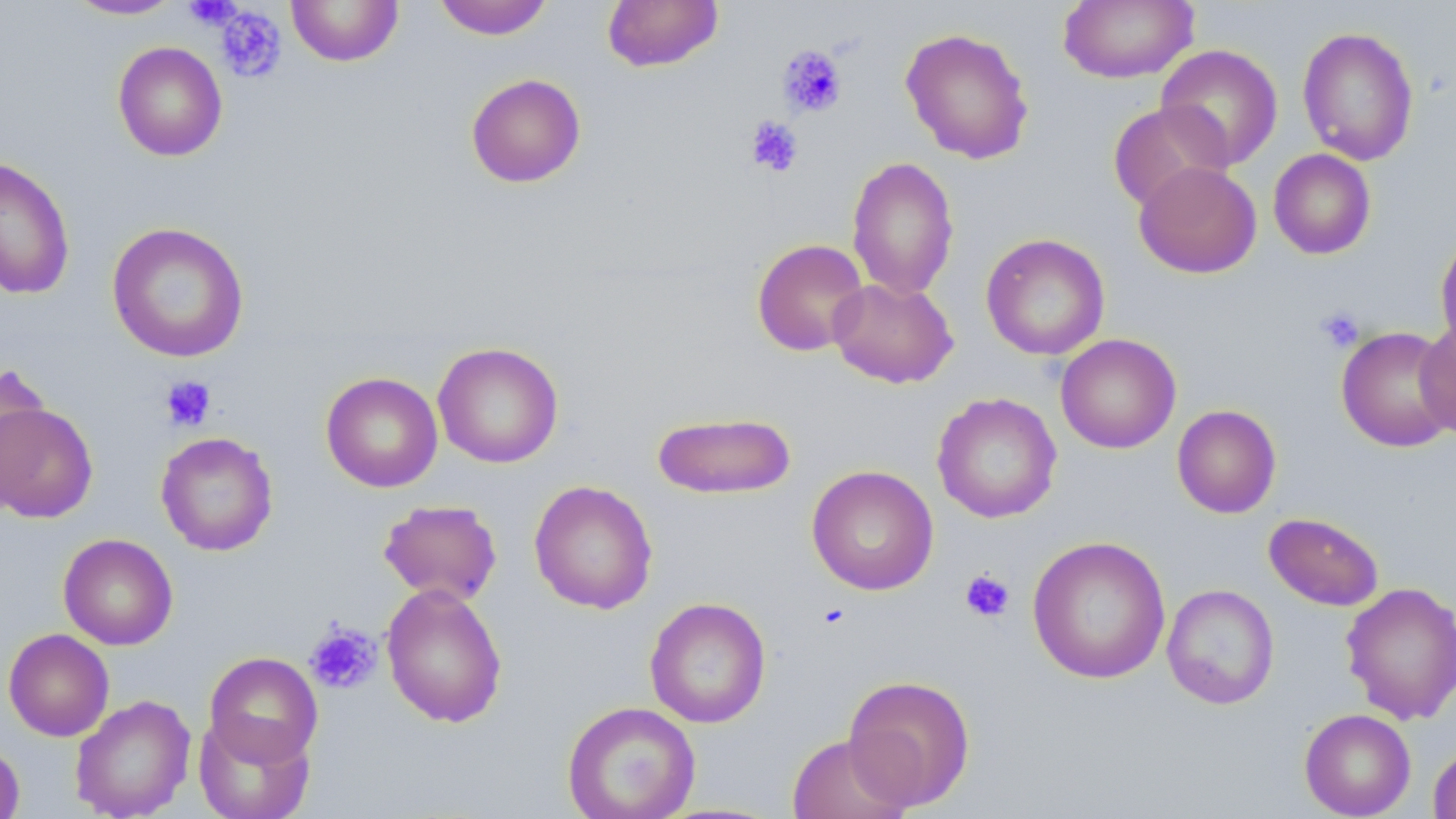

slide-level diagnosis = no evidence of blood parasites
uninfected red blood cell locations = approximate bounding boxes as (x1, y1, x2, y2) in pixels: (62, 0, 188, 21), (286, 0, 404, 67), (433, 0, 553, 40), (602, 0, 723, 72), (1057, 1, 1199, 84), (1297, 25, 1420, 166), (900, 27, 1035, 165), (112, 41, 228, 161), (1156, 43, 1284, 170), (465, 73, 586, 188), (1106, 101, 1233, 213), (1268, 149, 1377, 260), (0, 155, 75, 300), (846, 155, 959, 301), (1133, 161, 1262, 279), (106, 222, 249, 363), (1435, 232, 1456, 356), (980, 233, 1110, 360), (751, 238, 869, 356), (828, 277, 959, 389), (1416, 318, 1456, 444), (1335, 325, 1456, 453), (1055, 333, 1181, 453), (433, 341, 564, 468), (0, 364, 49, 503), (320, 372, 443, 492), (932, 392, 1062, 524), (0, 399, 99, 523), (1172, 404, 1281, 518), (652, 411, 797, 499), (155, 431, 278, 556), (806, 464, 939, 596), (529, 480, 658, 614), (379, 499, 503, 605), (1263, 512, 1384, 611), (58, 533, 178, 650), (1027, 536, 1171, 685), (1341, 581, 1456, 725), (381, 582, 508, 728), (1162, 583, 1279, 710), (644, 597, 771, 728), (3, 628, 114, 741), (204, 651, 323, 766), (842, 674, 976, 811), (70, 694, 196, 819), (562, 701, 701, 819), (1299, 708, 1416, 818), (193, 713, 315, 819), (787, 733, 912, 819), (0, 739, 25, 819), (1427, 742, 1456, 819)
field of view = one of a larger specimen
image size = 1456×819 pixels
stain = May-Grünwald-Giemsa
modality = light microscopy
platelet locations = approximate bounding boxes as (x1, y1, x2, y2) in pixels: (184, 0, 243, 30), (214, 5, 287, 83), (777, 45, 847, 117), (745, 116, 803, 177), (1315, 306, 1365, 354), (160, 375, 216, 432), (959, 569, 1015, 623), (816, 602, 851, 630), (305, 622, 382, 694)
preparation = thin blood film
magnification = 1000x